Locate every leukocyte (white blood cell).
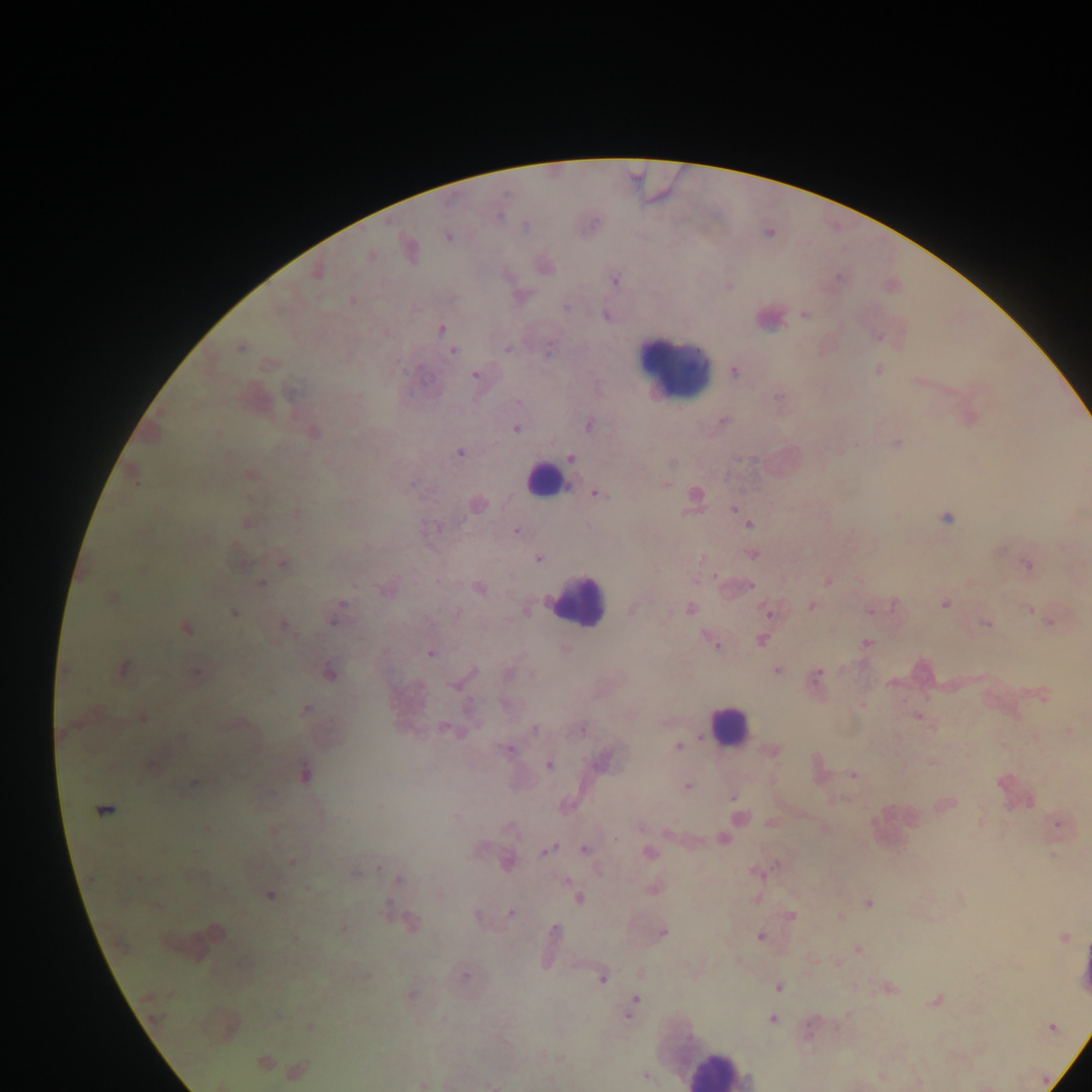

Approximate centers as {x, y} in pixels.
Leukocytes: {763, 320}, {675, 371}, {546, 481}, {574, 600}, {728, 728}, {894, 827}, {1083, 973}, {717, 1070}.

Malaria parasite locations: {526, 226}, {447, 235}, {409, 251}, {369, 255}, {544, 265}, {315, 271}, {614, 281}, {728, 286}, {520, 296}, {352, 300}, {804, 314}, {607, 315}, {440, 329}, {877, 336}, {240, 346}, {507, 348}, {452, 351}, {268, 364}, {876, 369}, {734, 370}, {475, 374}, {918, 380}, {969, 416}, {721, 420}, {589, 424}, {515, 427}, {313, 432}, {895, 443}, {459, 452}, {570, 458}, {671, 461}, {249, 474}, {133, 476}, {665, 484}, {595, 493}, {693, 494}, {476, 504}, {734, 508}, {295, 512}, {945, 517}, {245, 521}, {748, 523}, {437, 527}, {515, 529}, {752, 553}, {538, 558}, {283, 562}, {240, 563}, {1027, 565}, {828, 580}, {262, 582}, {969, 582}, {478, 587}, {386, 588}, {110, 598}, {944, 603}, {811, 605}, {633, 608}, {872, 608}, {1030, 608}, {525, 609}, {689, 609}, {767, 610}, {233, 612}, {334, 612}, {1051, 622}, {986, 624}, {284, 626}, {185, 627}, {760, 639}, {714, 642}, {866, 643}, {564, 649}, {430, 653}, {121, 669}, {776, 670}, {196, 671}, {328, 672}, {815, 677}, {460, 682}, {1042, 694}, {861, 704}, {305, 709}, {918, 715}, {142, 717}, {240, 724}, {535, 728}, {448, 730}, {581, 730}, {1069, 731}, {677, 746}, {507, 749}, {772, 750}, {603, 760}, {932, 763}, {151, 765}, {548, 765}, {304, 772}, {853, 775}, {193, 782}, {686, 786}, {732, 797}, {944, 803}, {104, 809}, {456, 816}, {738, 818}, {980, 822}, {1057, 822}, {508, 827}, {206, 829}, {272, 829}, {723, 838}, {546, 849}, {584, 849}, {649, 852}, {1054, 854}, {292, 862}, {506, 862}, {755, 871}, {356, 872}, {398, 879}, {652, 888}, {269, 895}, {577, 898}, {756, 898}, {868, 902}, {511, 912}, {478, 916}, {791, 916}, {840, 917}, {408, 923}, {342, 928}, {554, 931}, {662, 932}, {216, 933}, {551, 936}, {1063, 936}, {759, 937}, {857, 949}, {640, 973}, {464, 975}, {602, 976}, {777, 986}, {887, 988}, {409, 995}, {936, 999}, {632, 1005}, {772, 1020}, {309, 1027}, {1051, 1027}, {263, 1062}, {285, 1068}, {296, 1071}, {645, 1075}, {881, 1076}, {918, 1082}, {421, 1084}, {490, 1085}. Collected in Ghana. Mobile-phone photograph taken through the microscope. Image is 1092×1092 pixels. Single field of view. Thick blood smear.